Point out each Plasmodium parasite.
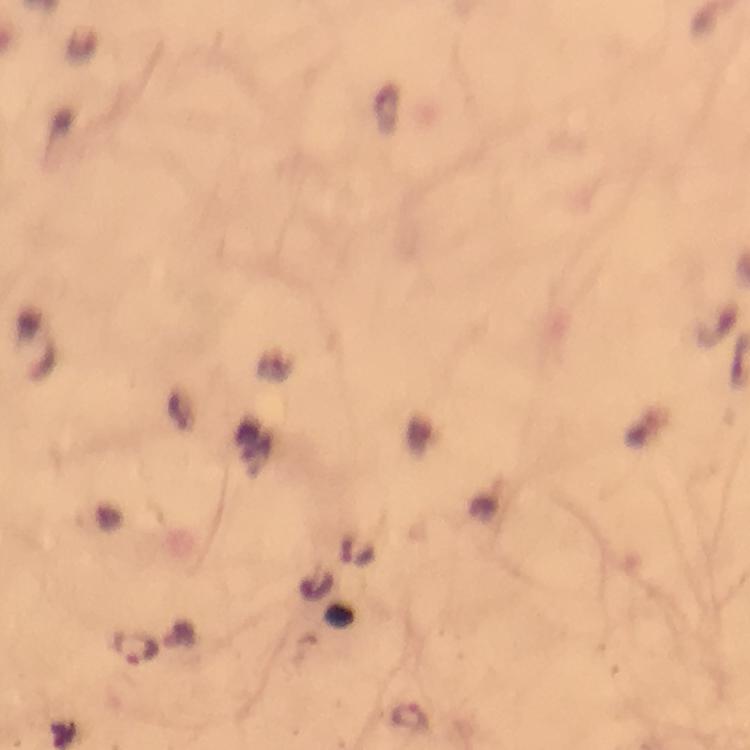
Approximate object centers, in pixels from the top-left corner.
Plasmodium parasites: (x=137, y=648), (x=413, y=720).

immersion oil = used
stain = Giemsa
capture = smartphone mounted on the microscope
image size = 750×750 pixels
context = from a diagnostic examination for malaria
preparation = thick blood film
cropped from = one field of view
magnification = 100x